Identify the cell.
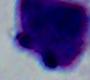

This is a leukocyte.

Captured at 1000x magnification. Photomicrograph.